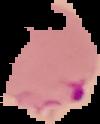
{
  "preparation": "thin blood film",
  "result": "Plasmodium parasites identified",
  "image_type": "cell region segmented out of the field of view; surrounding area masked to black",
  "image_size": "100×124 pixels"
}